Give the extent of all Plasmodium parasites.
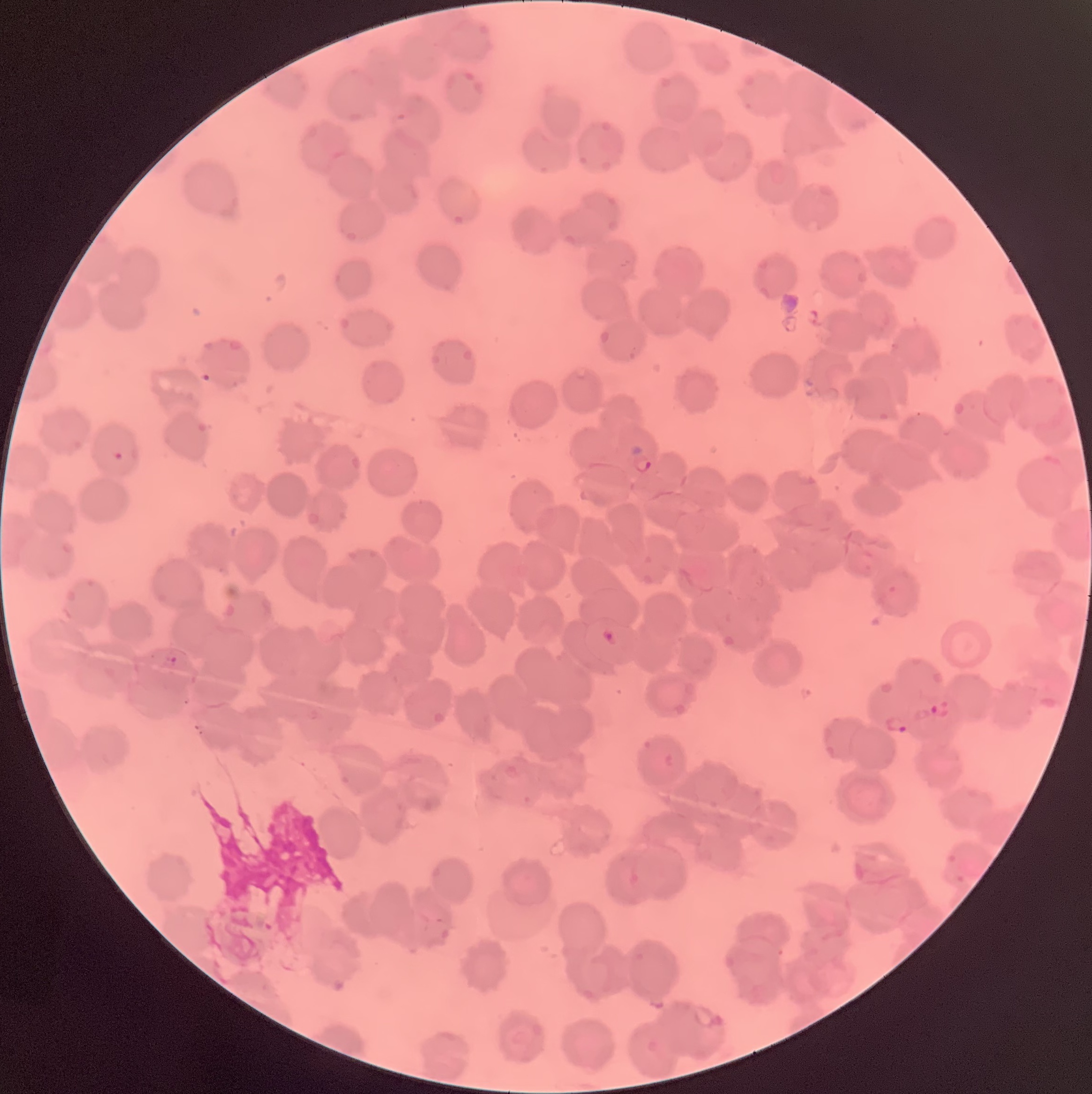

Approximate bounding boxes as named x1/y1/x2/y2 corners in pixels.
Plasmodium parasites: (x1=200, y1=371, x2=218, y2=384), (x1=112, y1=449, x2=139, y2=463), (x1=630, y1=453, x2=654, y2=474), (x1=601, y1=628, x2=619, y2=647), (x1=162, y1=656, x2=178, y2=669), (x1=929, y1=700, x2=953, y2=719), (x1=882, y1=715, x2=911, y2=735), (x1=692, y1=1003, x2=725, y2=1031).

Image is 1092×1094 pixels. Light microscopy. The red blood cells show rouleaux formation. Thin blood film.